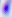 Toxoplasma gondii is shown. Micrograph. 400x magnification.